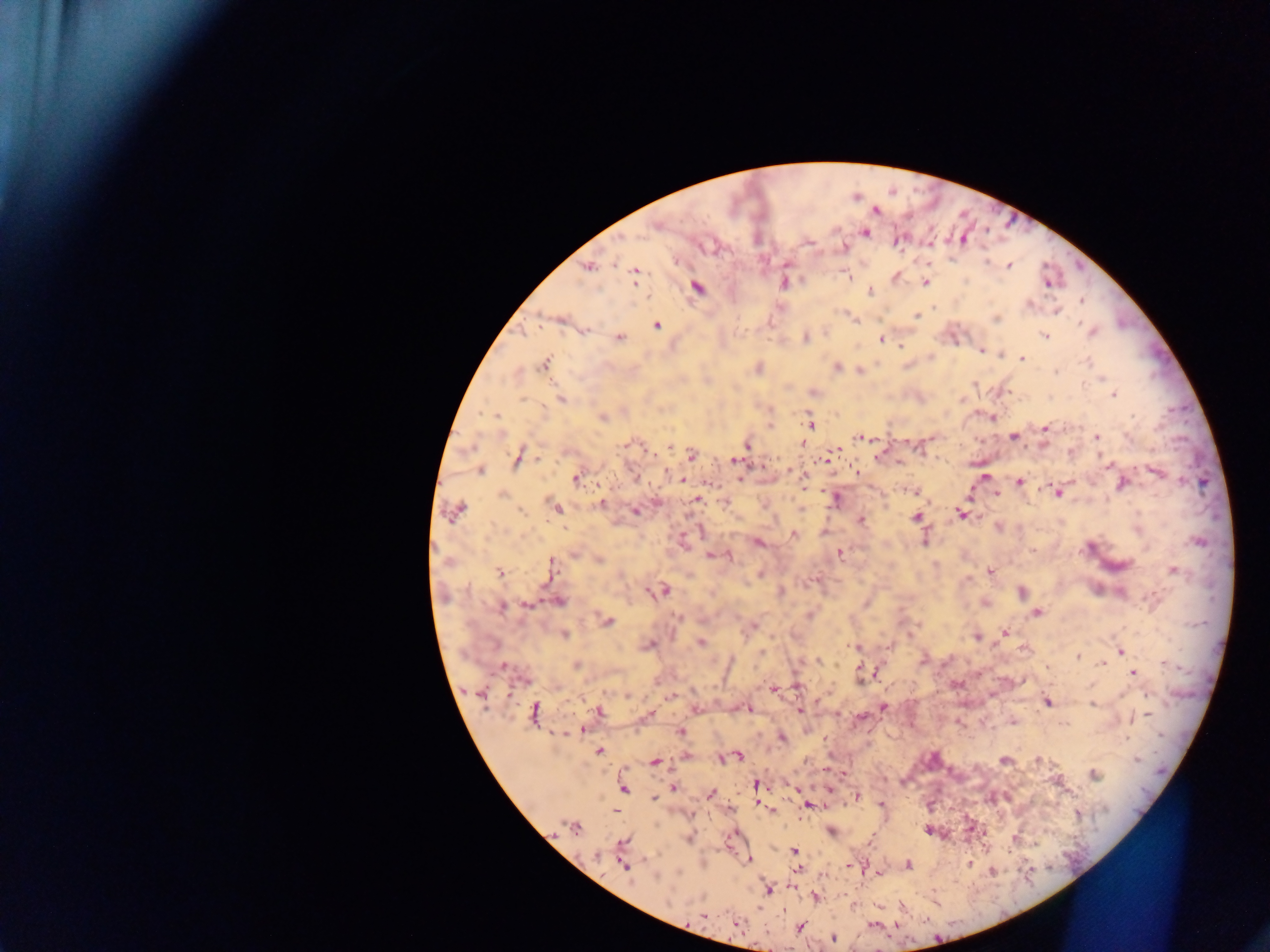

{
  "capture": "mobile-phone photograph through a microscope",
  "malaria_parasite_locations": "approximate centers as x y in pixels: 877 210; 655 226; 865 233; 964 238; 807 243; 898 243; 844 247; 786 264; 1009 266; 588 268; 634 274; 846 274; 925 283; 1048 283; 783 284; 697 287; 869 292; 1081 301; 1029 304; 1056 311; 917 316; 996 319; 657 325; 585 332; 1091 332; 1045 335; 619 338; 805 338; 881 339; 900 345; 981 351; 1022 358; 1088 362; 545 364; 837 366; 758 368; 1056 372; 1100 379; 974 384; 1114 395; 560 398; 962 398; 494 415; 603 418; 810 425; 769 426; 1044 428; 1014 437; 1097 437; 859 438; 628 444; 803 444; 670 446; 747 446; 835 449; 691 456; 518 457; 878 458; 826 459; 735 461; 900 462; 1108 464; 480 470; 666 471; 790 471; 1156 471; 856 472; 795 473; 635 477; 985 477; 576 478; 682 481; 805 481; 1019 482; 1122 484; 913 491; 1058 492; 503 494; 997 495; 835 499; 697 500; 725 502; 602 503; 555 508; 521 510; 636 511; 456 513; 961 514; 916 517; 861 520; 794 534; 923 540; 1198 542; 759 543; 1089 547; 1032 550; 840 554; 575 555; 713 555; 727 557; 600 560; 550 569; 990 571; 500 572; 1174 572; 811 581; 664 591; 650 592; 1021 592; 781 593; 559 602; 527 604; 866 604; 502 607; 1037 612; 677 616; 608 621; 753 627; 1003 632; 564 635; 910 635; 976 637; 700 642; 650 645; 852 647; 888 647; 1121 651; 1078 656; 818 661; 1102 664; 576 665; 503 667; 875 672; 1132 673; 860 675; 773 689; 797 689; 478 693; 672 696; 1048 702; 1091 704; 884 708; 748 709; 800 711; 533 712; 598 712; 1147 714; 648 716; 861 716; 1013 721; 1063 724; 583 730; 681 731; 782 738; 599 751; 738 756; 686 757; 727 758; 720 759; 1003 760; 1137 760; 655 761; 1093 775; 755 784; 674 788; 624 789; 710 793; 857 796; 654 799; 881 804; 759 805; 807 805; 771 810; 614 811; 574 828; 831 831; 688 839; 624 841; 794 850; 598 855; 748 860; 969 863; 908 865; 625 866; 849 866; 797 869; 993 871; 768 890; 816 897; 702 916; 737 923; 800 928; 833 938",
  "field_of_view": "single",
  "country": "Ghana",
  "preparation": "thick blood smear",
  "image_size": "1270×952 pixels"
}